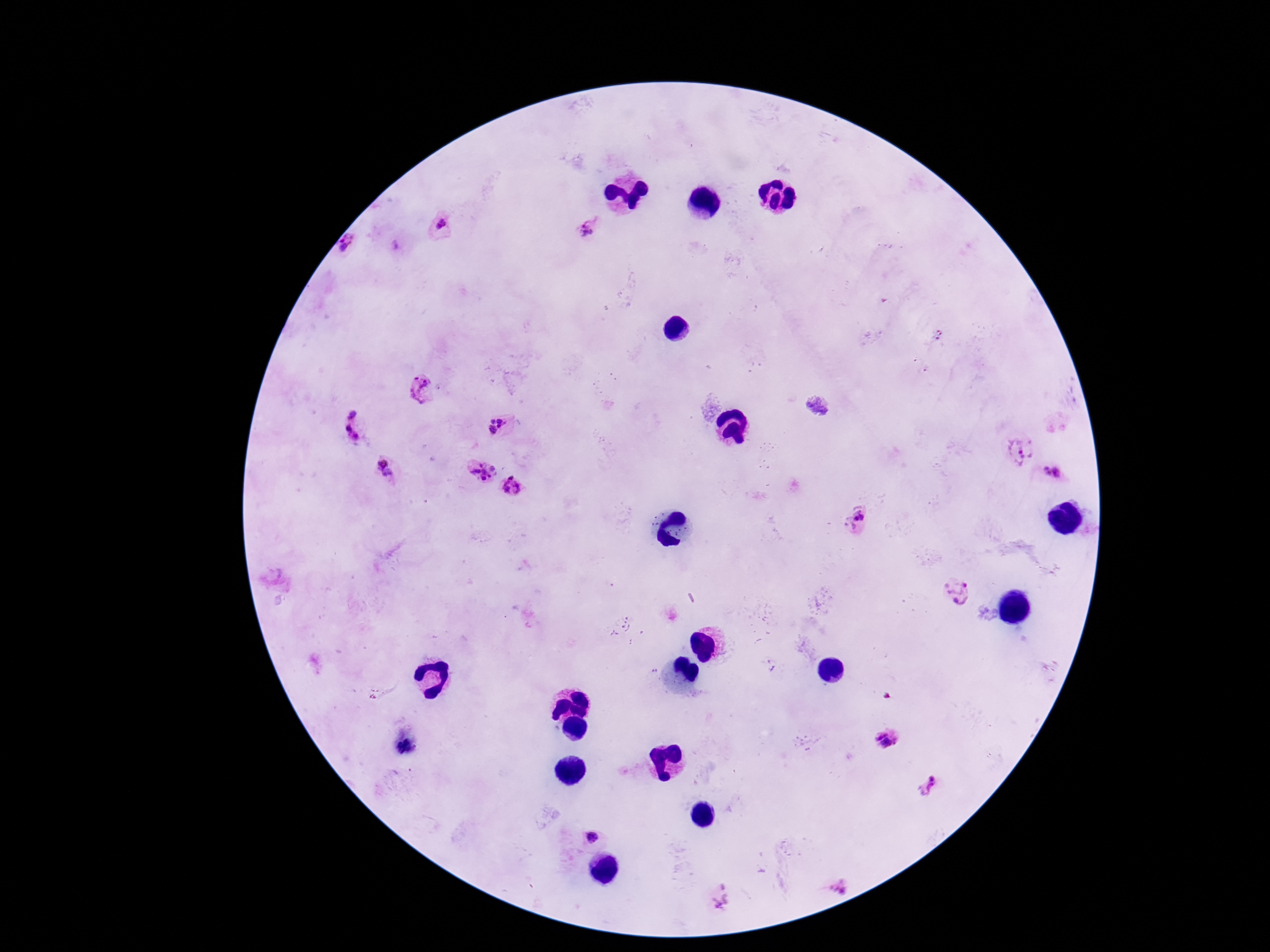

Approximate object centers, in pixels from the top-left corner. Plasmodium parasite locations: (x=442, y=224), (x=587, y=229), (x=349, y=244), (x=396, y=246), (x=938, y=335), (x=423, y=391), (x=818, y=404), (x=352, y=415), (x=497, y=426), (x=347, y=430), (x=357, y=437), (x=1021, y=452), (x=386, y=469), (x=484, y=472), (x=1058, y=472), (x=1047, y=473), (x=512, y=487), (x=859, y=520), (x=956, y=592), (x=886, y=739), (x=928, y=788), (x=592, y=837), (x=839, y=885), (x=721, y=896). Photographed through the microscope eyepiece with a smartphone camera. Giemsa stain. Patient malaria status: infected. Image is 1270×952 pixels. Thick peripheral-blood smear. One field from this slide. 100x magnification.